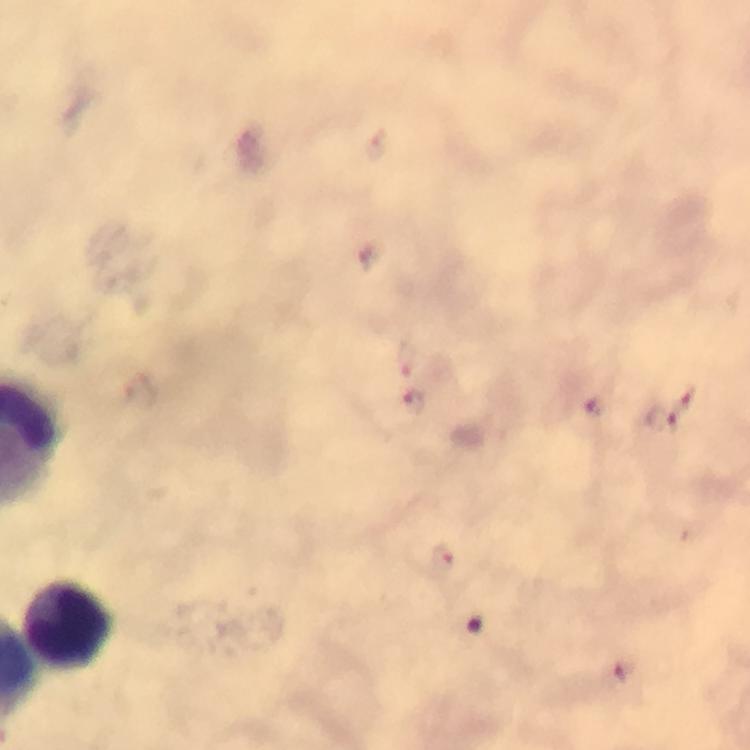

{
  "leukocyte_locations": "approximate centers as (x, y) in pixels: (71, 623)",
  "stain": "Giemsa",
  "plasmodium_parasite_locations": "approximate centers as (x, y) in pixels: (408, 359), (417, 399), (689, 400), (594, 407), (658, 418), (444, 560), (627, 670)",
  "image_size": "750×750 pixels",
  "context": "from a diagnostic examination for malaria",
  "immersion_oil": "used",
  "capture": "smartphone camera through the microscope",
  "cropped_from": "one field of view",
  "magnification": "100x",
  "preparation": "thick smear"
}